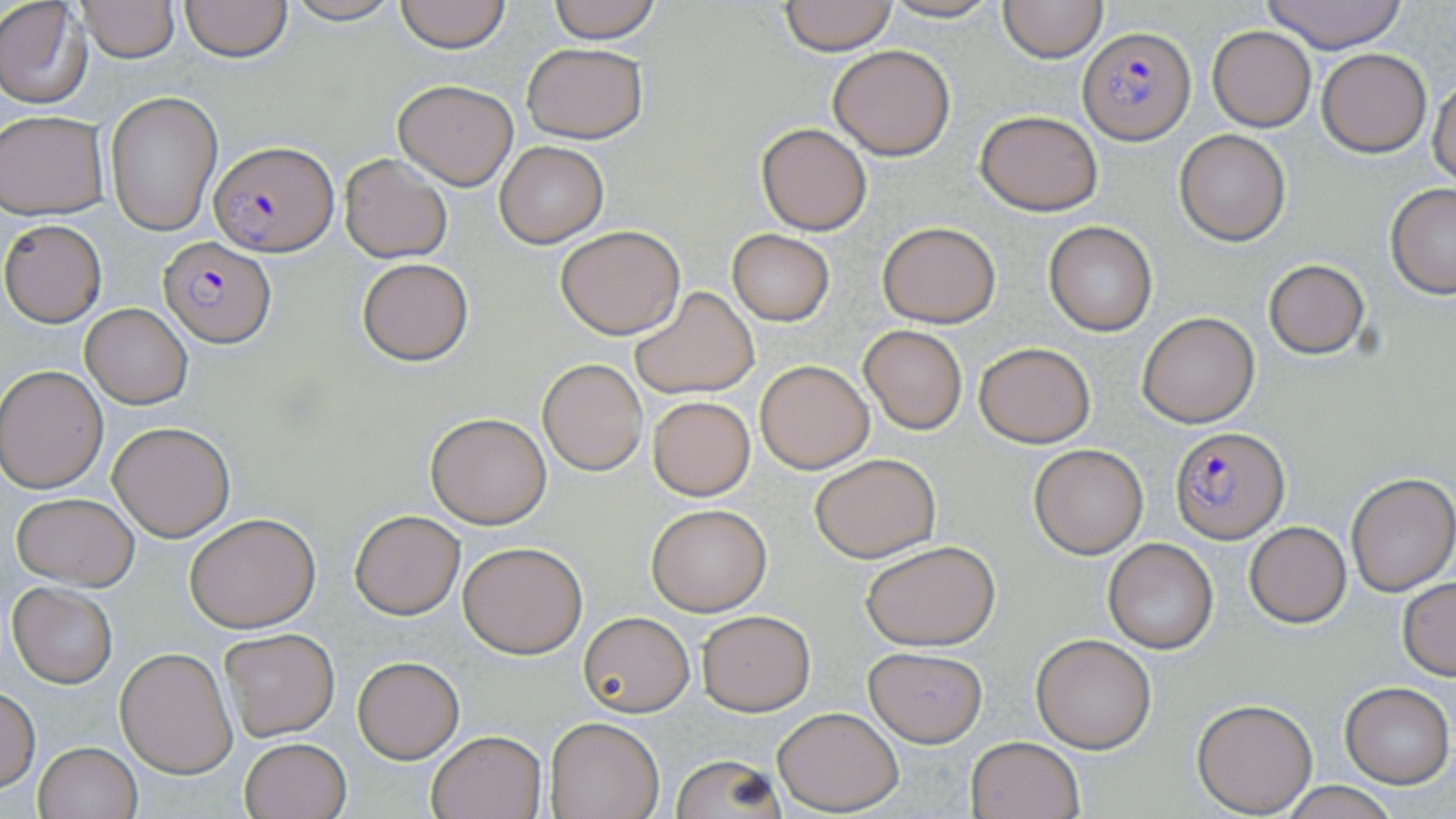
Summary:
  - Coordinate format: approximate bounding boxes as [x1, y1, x2, y2] in pixels
  - Plasmodium falciparum-infected red blood cell locations: [1081, 27, 1194, 144], [209, 142, 338, 258], [158, 237, 277, 348], [1170, 425, 1290, 543]
  - Uninfected red blood cell locations: [76, 0, 179, 61], [180, 0, 291, 61], [280, 0, 404, 25], [393, 0, 511, 52], [544, 0, 663, 44], [876, 0, 1006, 23], [998, 0, 1106, 62], [1259, 0, 1409, 53], [0, 1, 92, 108], [780, 1, 897, 53], [1207, 27, 1316, 131], [520, 42, 649, 144], [828, 44, 955, 160], [1317, 48, 1432, 157], [1429, 74, 1456, 185], [394, 78, 518, 188], [104, 92, 223, 235], [976, 109, 1103, 215], [1, 110, 109, 219], [754, 122, 872, 235], [1175, 129, 1291, 245], [493, 140, 609, 249], [340, 154, 452, 263], [1386, 183, 1456, 298], [1, 218, 107, 326], [876, 220, 1002, 328], [1042, 221, 1158, 336], [555, 225, 684, 339], [727, 229, 835, 325], [356, 256, 474, 366], [1261, 257, 1371, 361], [630, 287, 760, 398], [80, 303, 194, 409], [1136, 312, 1259, 428], [859, 324, 968, 435], [975, 342, 1095, 447], [537, 358, 648, 475], [755, 358, 874, 473], [0, 366, 108, 493], [647, 395, 755, 500], [426, 412, 551, 528], [108, 421, 236, 541], [1029, 444, 1147, 557], [810, 453, 941, 562], [1346, 471, 1456, 596], [12, 492, 138, 590], [647, 503, 771, 616], [349, 508, 465, 620], [184, 513, 320, 633], [1244, 521, 1351, 628], [1103, 538, 1218, 654], [860, 539, 1000, 650], [458, 540, 587, 658], [1396, 578, 1456, 680], [8, 583, 117, 687], [696, 610, 816, 715], [578, 611, 694, 717], [219, 628, 341, 741], [1031, 634, 1157, 753], [115, 646, 237, 777], [863, 646, 988, 746], [351, 654, 466, 764], [1339, 682, 1454, 787], [0, 689, 40, 792], [1193, 698, 1317, 816], [773, 705, 904, 814], [545, 717, 666, 819], [426, 730, 546, 818], [966, 736, 1086, 819], [240, 737, 352, 819], [33, 741, 142, 819], [668, 754, 788, 819], [1276, 781, 1400, 819]
  - Slide-level diagnosis: Plasmodium falciparum
  - Image size: 1456×819 pixels
  - Stain: May-Grünwald-Giemsa
  - Preparation: thin blood film
  - Field of view: one of a larger specimen
  - Modality: light microscopy
  - Magnification: 1000x